State the preparation type.
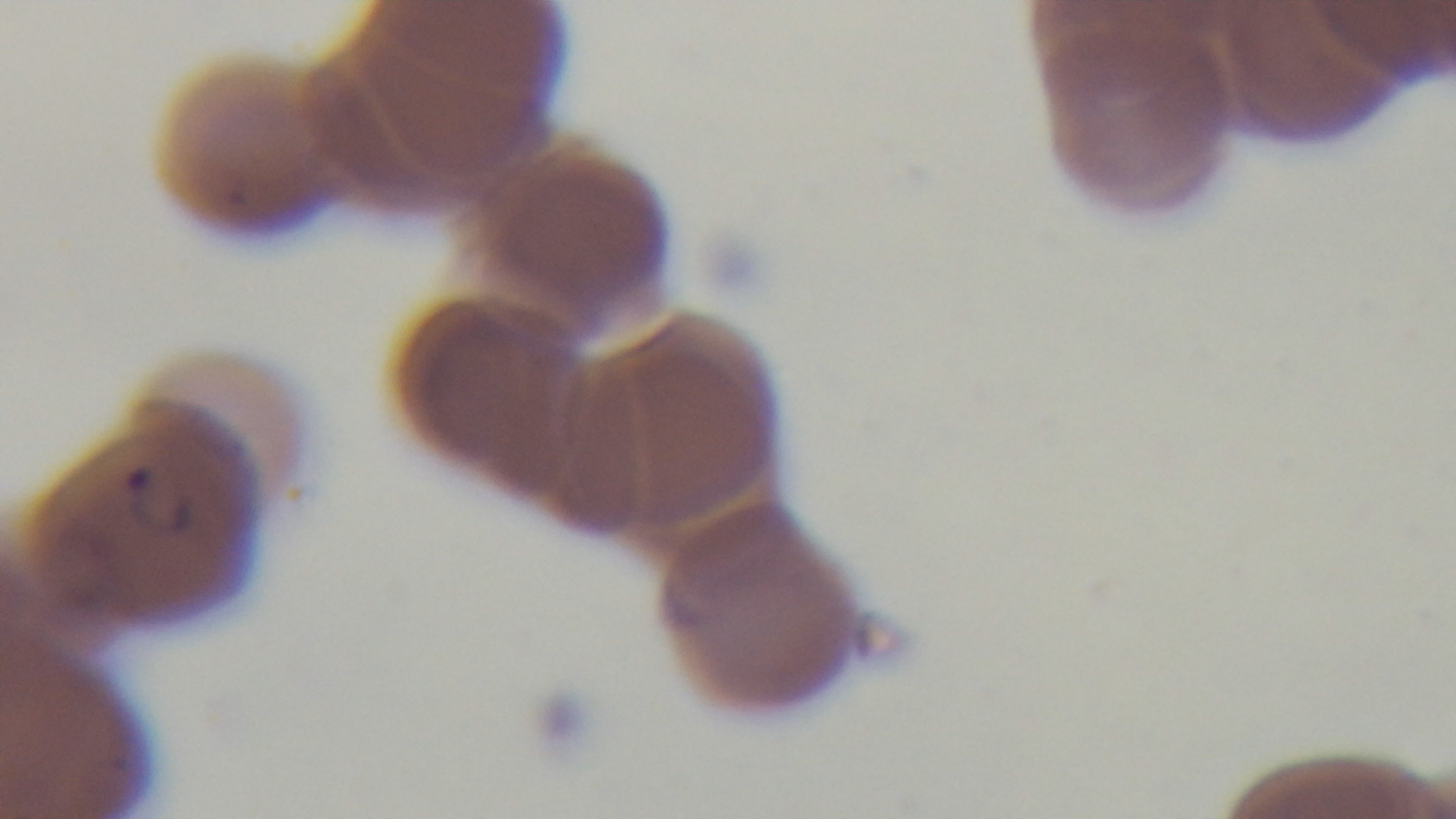

Thin.

Summary:
  - Modality: light microscopy
  - Objective: 100x oil immersion
  - Capture: mounted 4K digital camera
  - Field of view: single
  - Malaria status: infected
  - Stain: Giemsa